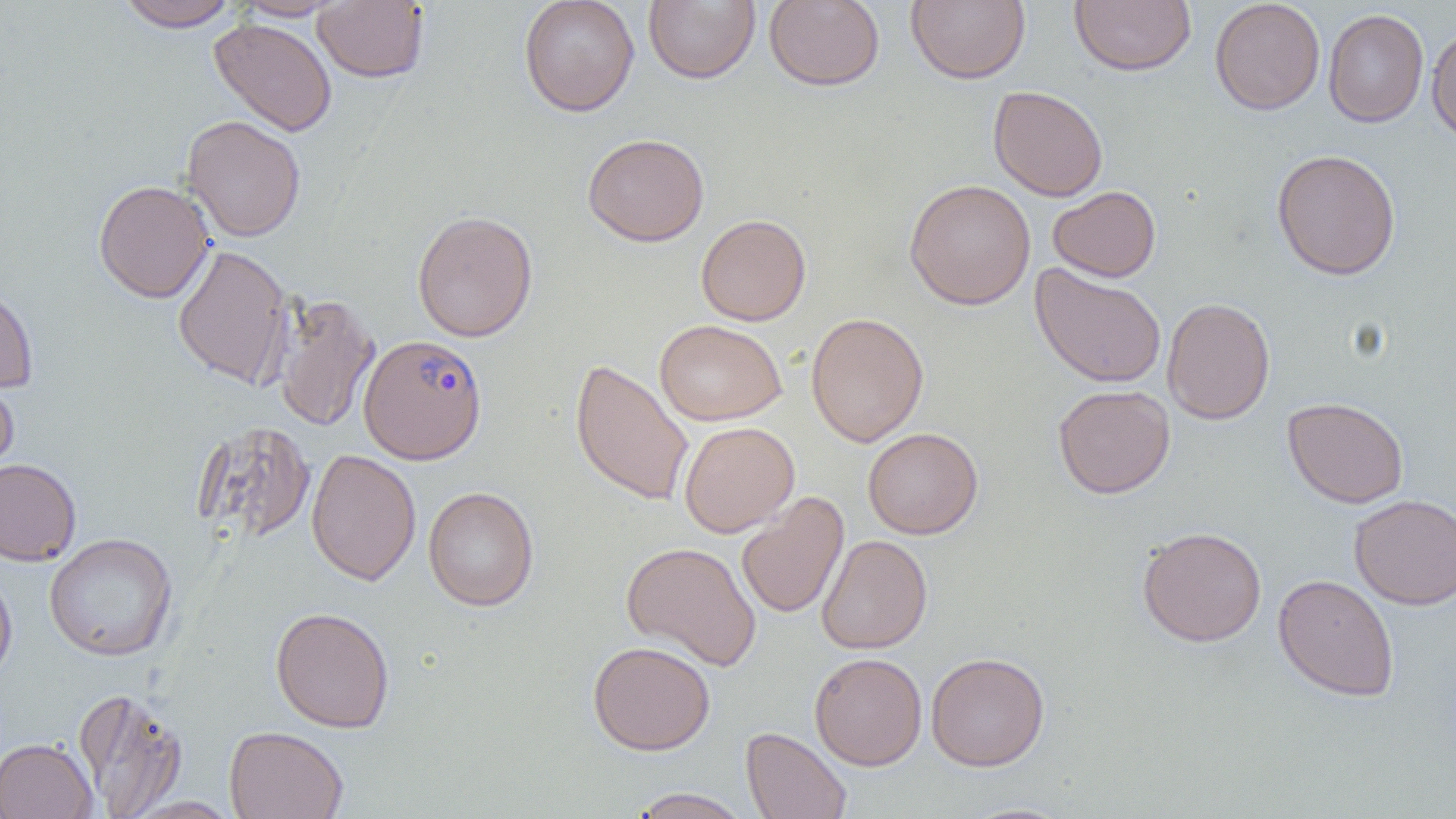

Summary:
  - Coordinate format: approximate bounding boxes as named x1/y1/x2/y2 corners in pixels
  - Plasmodium falciparum-infected red blood cell locations: (x1=359, y1=334, x2=487, y2=464)
  - Uninfected red blood cell locations: (x1=234, y1=0, x2=349, y2=21), (x1=518, y1=0, x2=640, y2=117), (x1=764, y1=0, x2=885, y2=91), (x1=906, y1=0, x2=1030, y2=84), (x1=1070, y1=0, x2=1196, y2=76), (x1=1210, y1=0, x2=1325, y2=115), (x1=115, y1=1, x2=242, y2=32), (x1=312, y1=1, x2=429, y2=83), (x1=644, y1=1, x2=761, y2=84), (x1=1323, y1=9, x2=1429, y2=128), (x1=208, y1=18, x2=338, y2=137), (x1=1426, y1=24, x2=1456, y2=146), (x1=988, y1=85, x2=1108, y2=201), (x1=182, y1=115, x2=306, y2=242), (x1=582, y1=133, x2=709, y2=246), (x1=1271, y1=148, x2=1401, y2=280), (x1=904, y1=178, x2=1036, y2=310), (x1=93, y1=180, x2=214, y2=303), (x1=1048, y1=185, x2=1161, y2=282), (x1=412, y1=210, x2=538, y2=342), (x1=695, y1=214, x2=811, y2=326), (x1=172, y1=244, x2=293, y2=389), (x1=1029, y1=263, x2=1167, y2=388), (x1=0, y1=280, x2=39, y2=393), (x1=272, y1=294, x2=381, y2=433), (x1=1161, y1=297, x2=1275, y2=425), (x1=805, y1=312, x2=929, y2=447), (x1=655, y1=319, x2=786, y2=425), (x1=569, y1=358, x2=694, y2=506), (x1=0, y1=372, x2=20, y2=480), (x1=1052, y1=384, x2=1175, y2=499), (x1=1282, y1=396, x2=1409, y2=508), (x1=193, y1=421, x2=317, y2=544), (x1=679, y1=421, x2=799, y2=537), (x1=863, y1=427, x2=983, y2=539), (x1=306, y1=449, x2=421, y2=586), (x1=0, y1=458, x2=82, y2=566), (x1=423, y1=486, x2=539, y2=612), (x1=736, y1=492, x2=849, y2=620), (x1=1349, y1=494, x2=1456, y2=610), (x1=1136, y1=525, x2=1267, y2=648), (x1=44, y1=532, x2=178, y2=661), (x1=816, y1=534, x2=933, y2=654), (x1=621, y1=540, x2=762, y2=671), (x1=0, y1=566, x2=17, y2=686), (x1=1273, y1=573, x2=1400, y2=702), (x1=270, y1=606, x2=395, y2=733), (x1=587, y1=640, x2=715, y2=755), (x1=925, y1=651, x2=1050, y2=771), (x1=809, y1=653, x2=927, y2=770), (x1=73, y1=688, x2=188, y2=817), (x1=224, y1=726, x2=348, y2=819), (x1=741, y1=727, x2=852, y2=819), (x1=0, y1=738, x2=97, y2=819), (x1=629, y1=787, x2=752, y2=818), (x1=124, y1=796, x2=243, y2=818), (x1=956, y1=801, x2=1079, y2=819)
  - Slide-level diagnosis: Plasmodium falciparum
  - Image size: 1456×819 pixels
  - Preparation: thin blood smear
  - Field of view: one of a larger specimen
  - Magnification: 1000x
  - Modality: light microscopy